Locate every Plasmodium parasite.
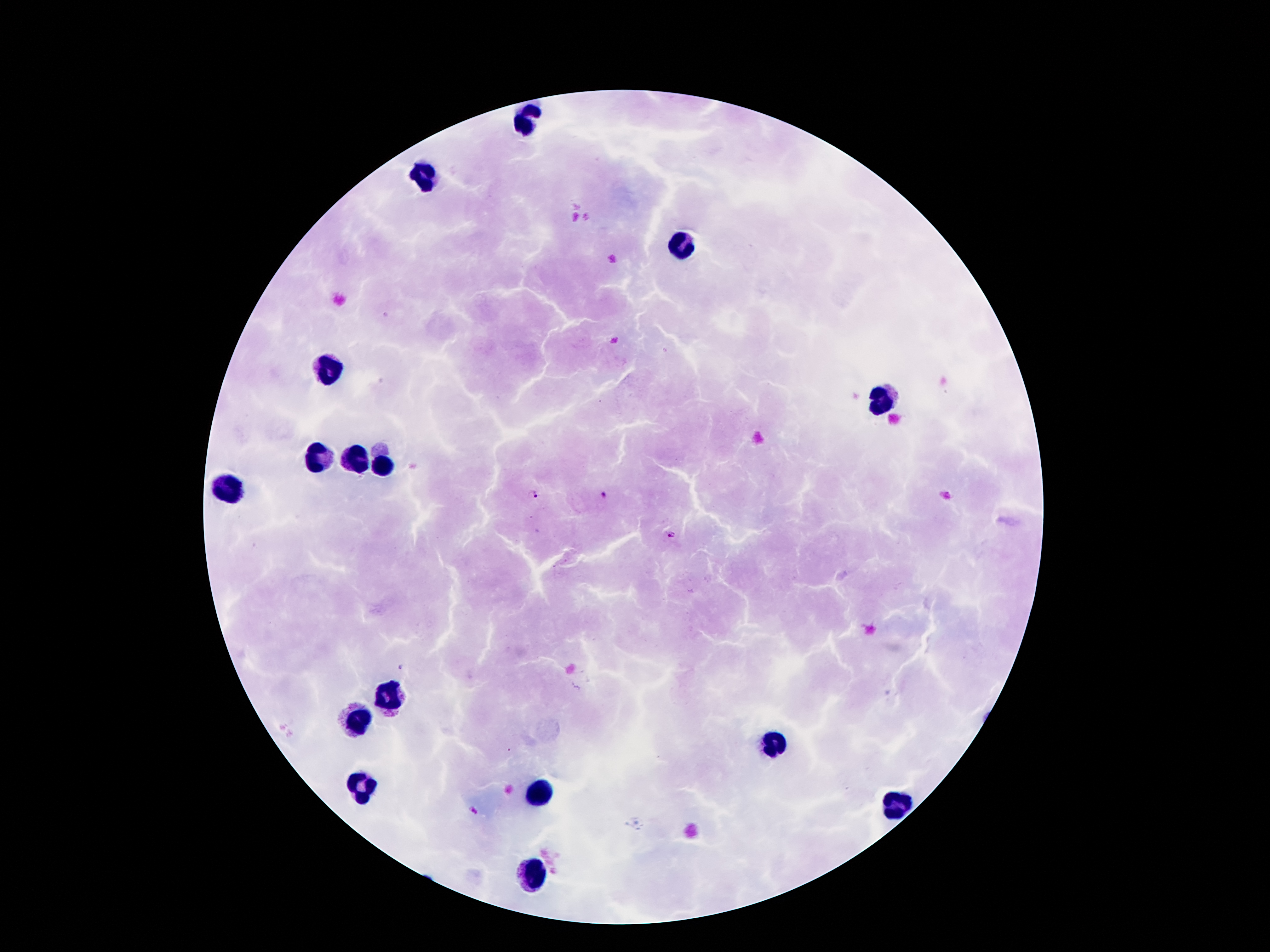

Approximate centers as {x, y} in pixels.
Plasmodium parasites: {532, 494}, {606, 495}, {671, 534}, {401, 667}, {472, 812}.

leukocyte locations = {526, 124}, {424, 178}, {681, 244}, {326, 368}, {883, 399}, {318, 459}, {353, 460}, {382, 468}, {229, 491}, {394, 698}, {355, 720}, {773, 743}, {356, 786}, {536, 794}, {893, 807}, {529, 875}
capture = smartphone camera through the microscope eyepiece
patient malaria status = infected with Plasmodium falciparum
magnification = 100x
preparation = thick blood film
stain = Giemsa
image size = 1270×952 pixels
field of view = single